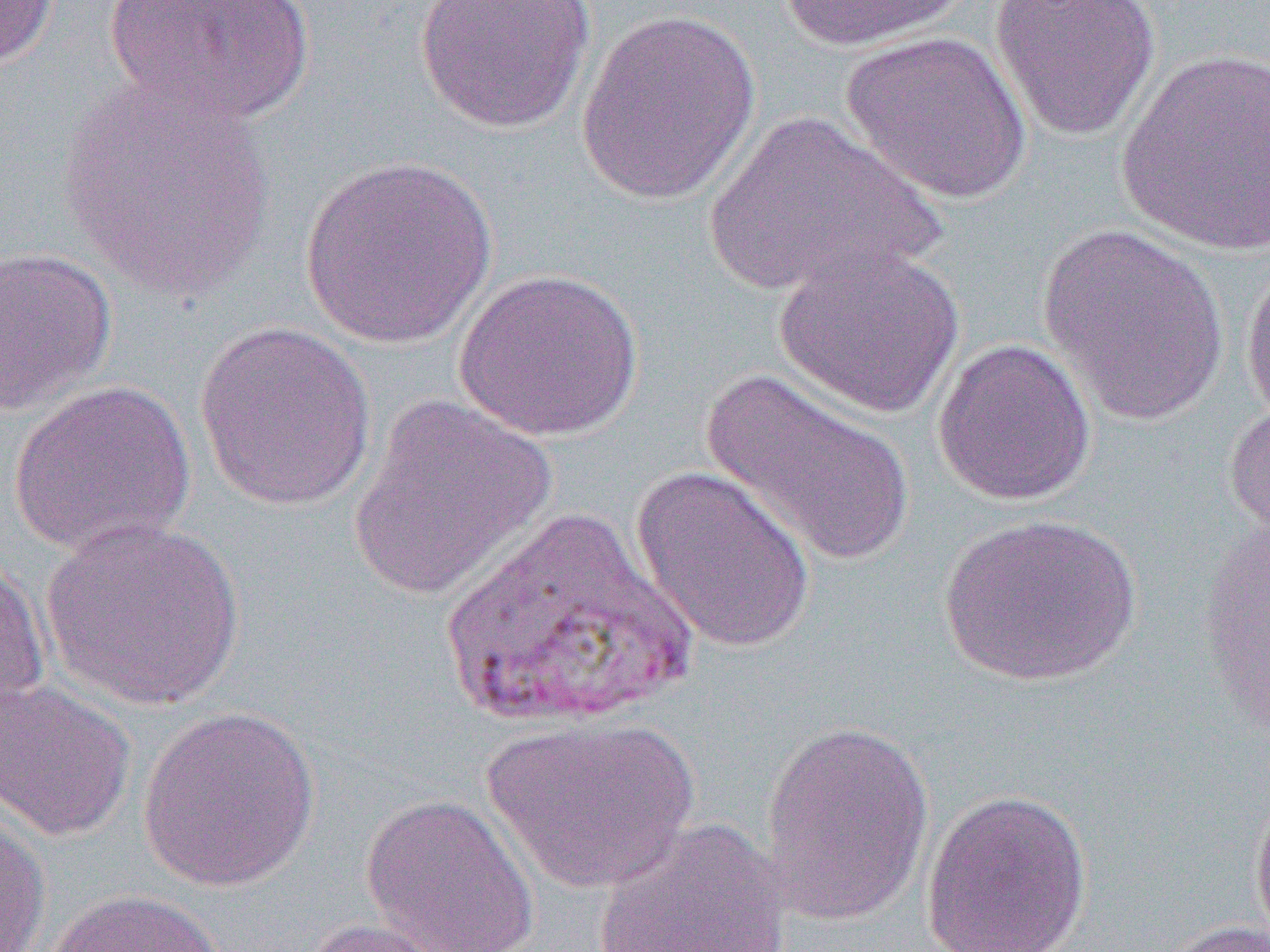
Approximate bounding boxes as named x1/y1/x2/y2 corners in pixels. Uninfected red blood cell locations: (x1=1, y1=0, x2=61, y2=69), (x1=102, y1=0, x2=317, y2=126), (x1=413, y1=0, x2=597, y2=134), (x1=780, y1=0, x2=971, y2=52), (x1=988, y1=0, x2=1161, y2=142), (x1=575, y1=7, x2=762, y2=205), (x1=840, y1=31, x2=1033, y2=204), (x1=1116, y1=49, x2=1270, y2=257), (x1=57, y1=71, x2=277, y2=303), (x1=700, y1=112, x2=945, y2=299), (x1=299, y1=154, x2=498, y2=349), (x1=1036, y1=225, x2=1231, y2=425), (x1=773, y1=244, x2=965, y2=419), (x1=0, y1=246, x2=118, y2=416), (x1=1240, y1=258, x2=1270, y2=427), (x1=453, y1=268, x2=645, y2=441), (x1=194, y1=322, x2=378, y2=513), (x1=932, y1=338, x2=1096, y2=507), (x1=702, y1=369, x2=914, y2=568), (x1=9, y1=379, x2=196, y2=558), (x1=347, y1=393, x2=559, y2=603), (x1=1222, y1=397, x2=1270, y2=544), (x1=630, y1=465, x2=817, y2=654), (x1=940, y1=512, x2=1140, y2=686), (x1=40, y1=517, x2=246, y2=712), (x1=1197, y1=517, x2=1270, y2=739), (x1=0, y1=553, x2=51, y2=713), (x1=0, y1=676, x2=136, y2=843), (x1=137, y1=705, x2=321, y2=893), (x1=483, y1=716, x2=700, y2=893), (x1=757, y1=718, x2=935, y2=926), (x1=918, y1=787, x2=1094, y2=952), (x1=1249, y1=789, x2=1270, y2=951), (x1=360, y1=792, x2=541, y2=951), (x1=0, y1=812, x2=51, y2=952), (x1=592, y1=816, x2=794, y2=951), (x1=45, y1=888, x2=227, y2=952), (x1=300, y1=917, x2=469, y2=952), (x1=1158, y1=918, x2=1269, y2=952). Slide-level diagnosis: Plasmodium vivax. Optical microscopy. Image is 1270×952 pixels. Thin blood film. 1000x magnification. Single field of view.